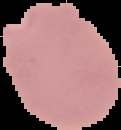
image size = 121×130 pixels
preparation = thin blood film
result = malaria parasites detected
image type = segmented cell region on a black background